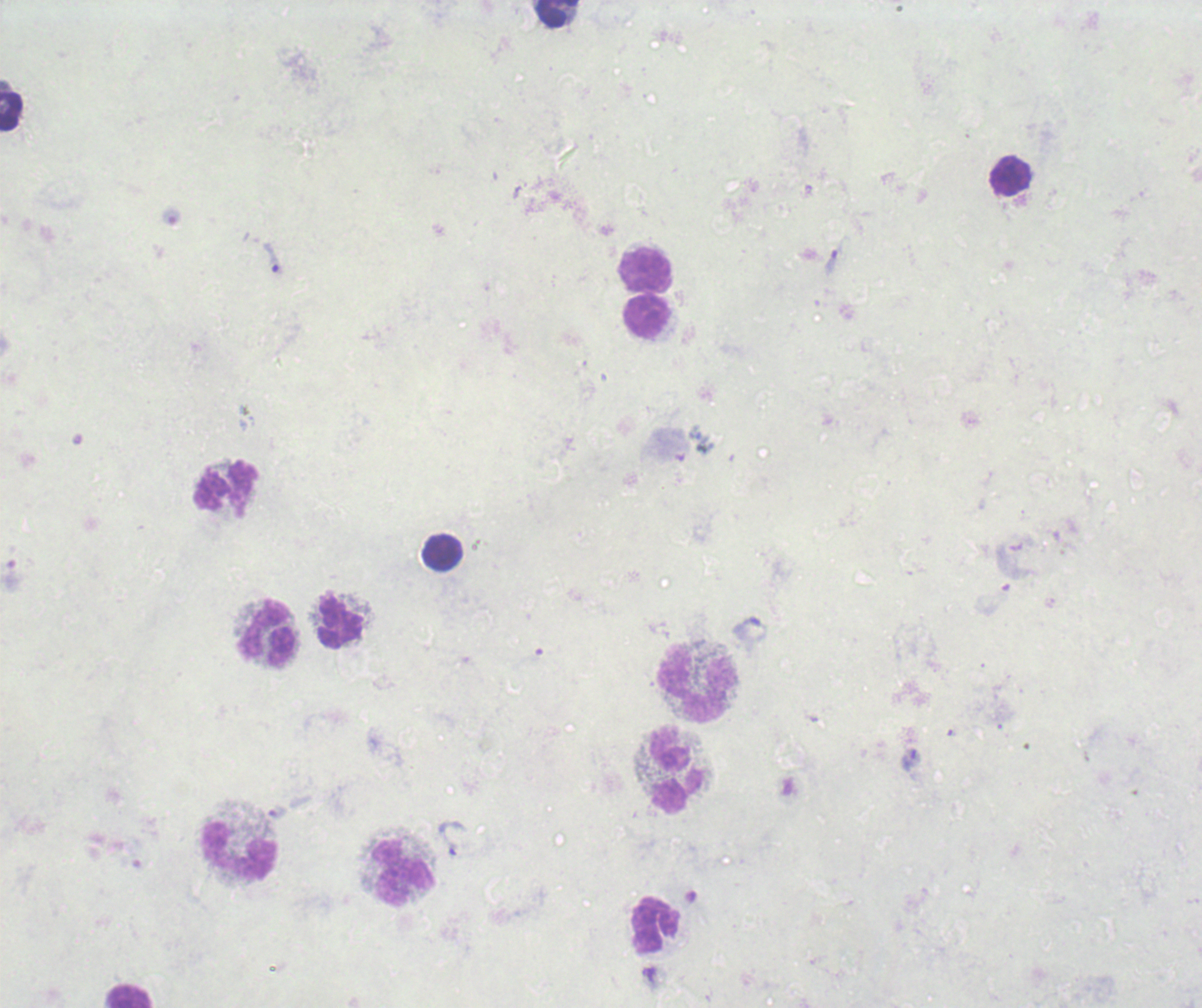

Approximate centers as (x, y) in pixels. Trophozoite locations: (838, 255), (273, 259), (277, 813), (452, 838). Leukocyte locations: (557, 14), (12, 108), (1010, 175), (646, 269), (647, 317), (226, 489), (443, 551), (340, 622), (267, 634), (697, 683), (675, 770), (238, 850), (404, 872), (655, 925), (129, 996). Romanowsky stain. Result: positive for Plasmodium parasites. Thick blood smear. Image is 1202×1008 pixels. Background quality: poor. Single field of view. Previously used in an actual diagnosis. 100x magnification.